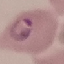
result = malaria parasites identified
preparation = thin smear
image type = cell patch, automatically extracted from a larger field of view and resized to 64 × 64 pixels
stain = Giemsa
capture = smartphone camera at the microscope eyepiece